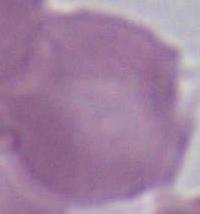 Captured at 1000x magnification. Photomicrograph. A red blood cell is seen.